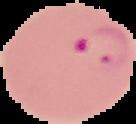
image type = segmented cell region with the area outside set to black
result = Plasmodium parasites detected
preparation = thin blood smear
image size = 136×124 pixels